Locate every Plasmodium parasite.
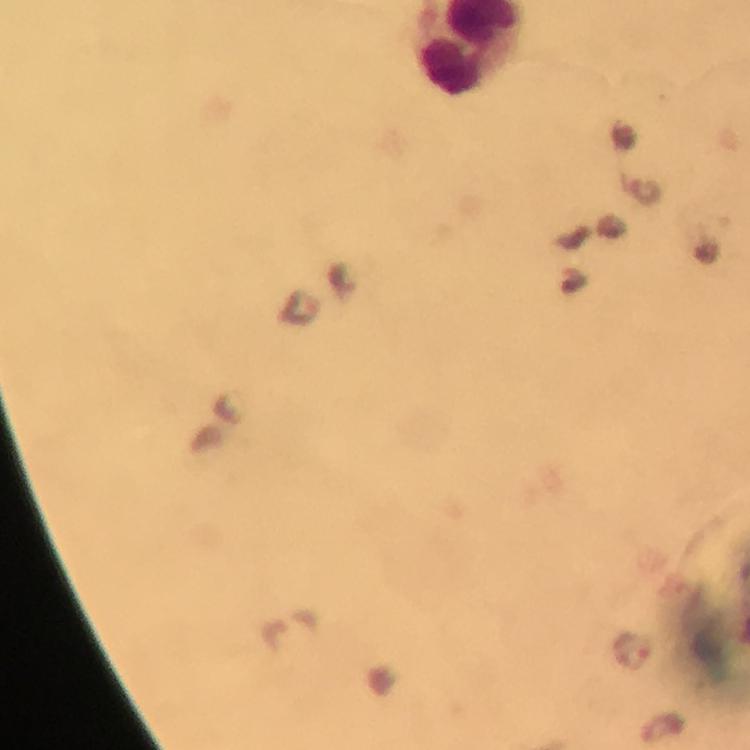
Approximate centers as {x, y} in pixels.
Plasmodium parasites: {646, 193}, {342, 280}, {297, 308}, {632, 651}.

100x magnification. Giemsa stain. Immersion oil applied. Photographed with a smartphone mounted on the microscope. Thick blood smear. From a malaria diagnostic workup. Image is 750×750 pixels. A crop from one field of view.